State the preparation type.
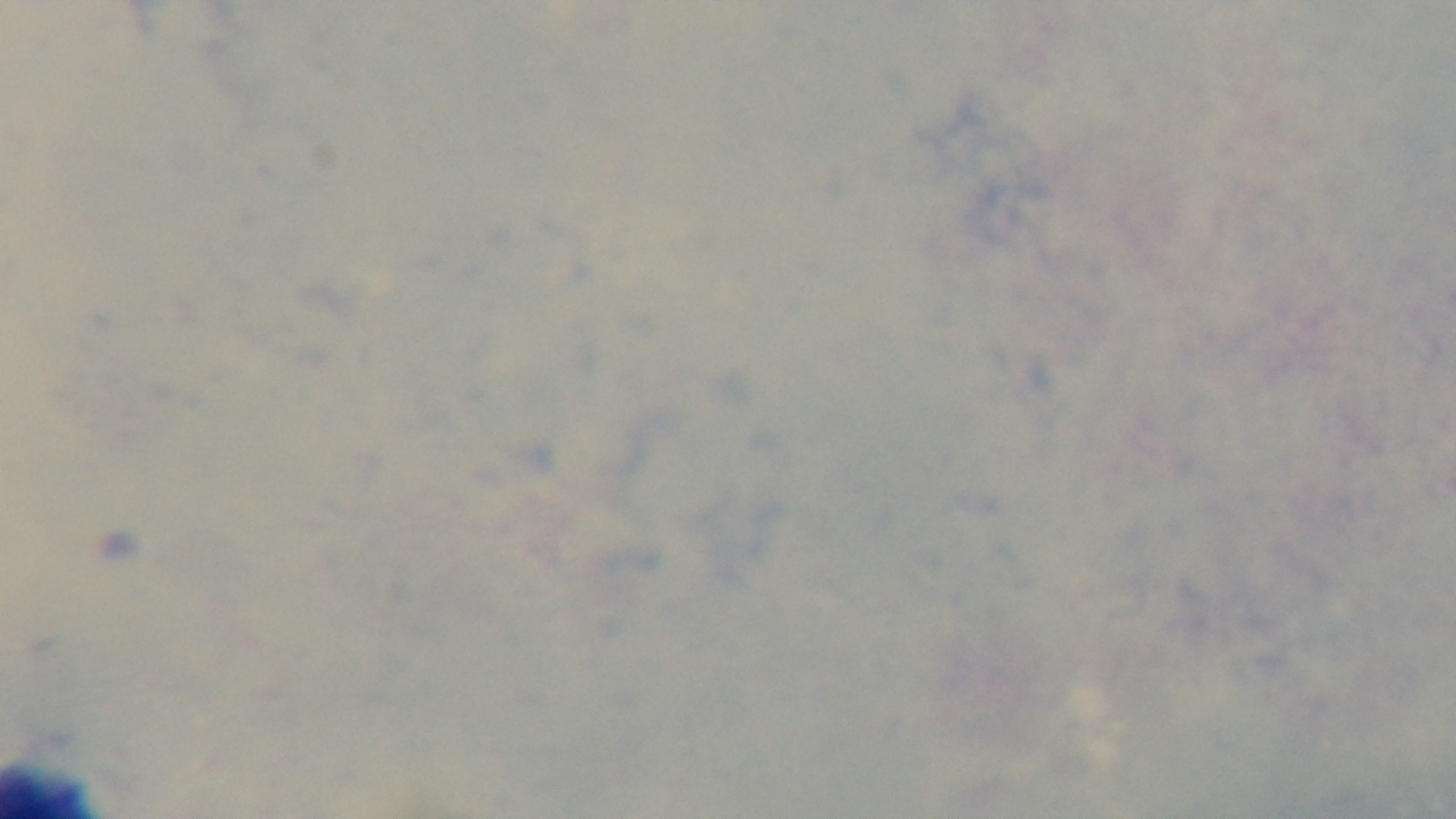
Thick.

Oil-immersion objective, 100x. Captured with a mounted 4K digital camera. Malaria status: uninfected. Giemsa stain. Light microscopy. Single field of view.